Name the blood parasite species.
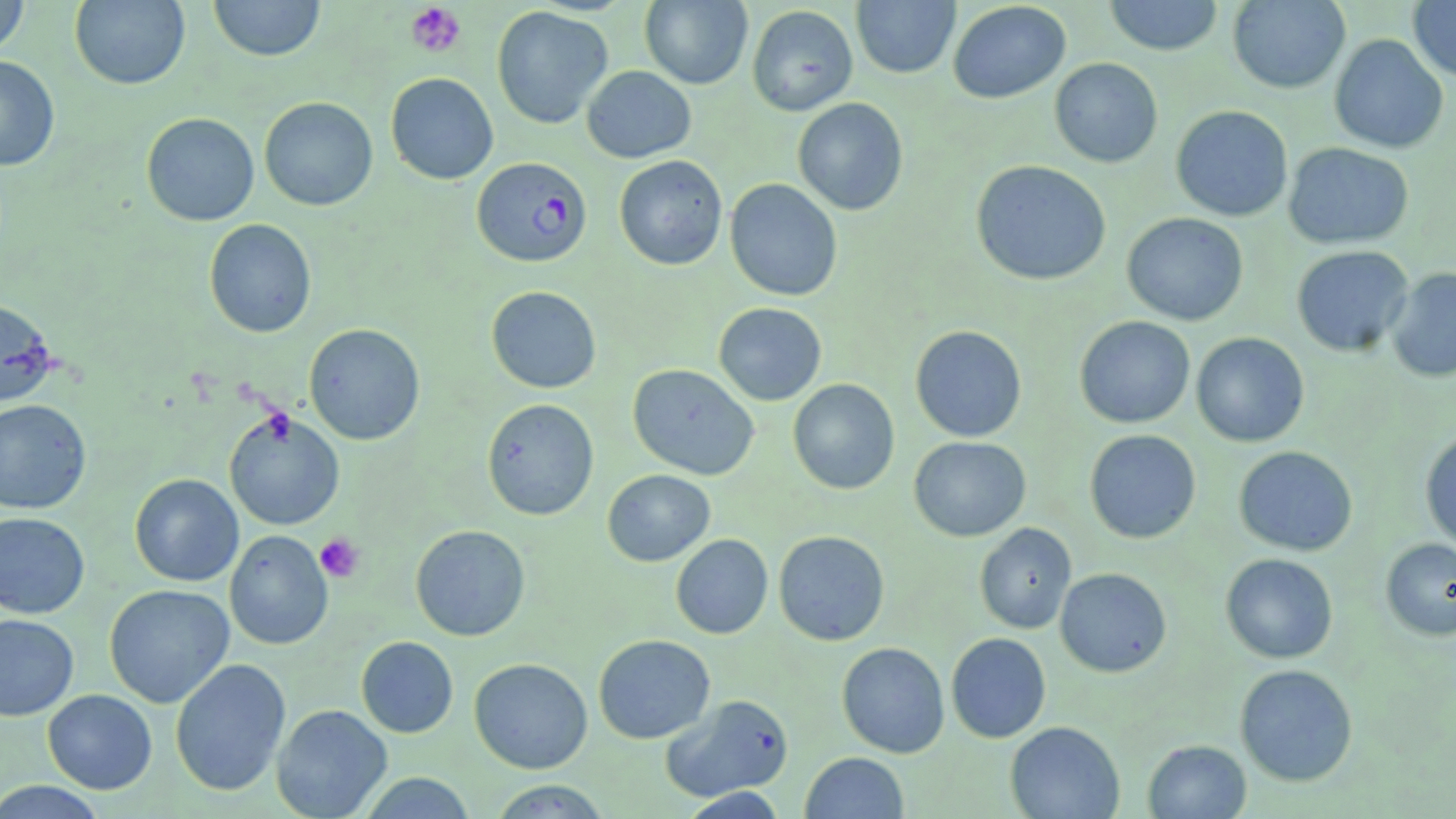
Plasmodium falciparum.

Summary:
  - Coordinate format: approximate bounding boxes as (x1, y1, x2, y2) in pixels
  - Plasmodium falciparum-infected red blood cell locations: (472, 158, 592, 268)
  - Uninfected red blood cell locations: (0, 0, 30, 58), (69, 0, 190, 90), (208, 0, 326, 62), (851, 0, 960, 79), (1104, 0, 1223, 56), (1227, 0, 1350, 94), (639, 1, 753, 89), (947, 1, 1071, 104), (1407, 1, 1456, 81), (491, 5, 612, 129), (747, 5, 858, 116), (1329, 33, 1449, 154), (0, 55, 60, 171), (1049, 57, 1163, 168), (581, 65, 696, 163), (385, 72, 498, 185), (258, 97, 378, 211), (792, 98, 908, 216), (1170, 105, 1293, 222), (141, 112, 260, 226), (1283, 142, 1414, 249), (614, 155, 728, 270), (970, 160, 1112, 286), (724, 178, 843, 301), (1121, 212, 1249, 326), (203, 218, 316, 338), (1290, 245, 1414, 357), (1387, 267, 1456, 383), (486, 285, 601, 393), (0, 297, 58, 407), (713, 302, 827, 406), (1074, 316, 1195, 428), (304, 323, 425, 445), (909, 325, 1027, 442), (1190, 332, 1309, 448), (628, 363, 759, 480), (787, 378, 900, 495), (482, 398, 599, 521), (0, 399, 92, 514), (224, 410, 345, 530), (1084, 429, 1201, 543), (1420, 429, 1456, 551), (908, 436, 1031, 541), (1233, 446, 1358, 556), (602, 469, 715, 567), (129, 474, 243, 586), (0, 511, 90, 618), (974, 522, 1077, 634), (410, 524, 530, 641), (224, 530, 333, 650), (773, 530, 890, 646), (671, 534, 773, 639), (1380, 537, 1456, 642), (1220, 553, 1338, 663), (1055, 568, 1172, 677), (104, 584, 234, 708), (0, 614, 79, 720), (946, 632, 1051, 743), (593, 634, 715, 744), (356, 636, 458, 738), (836, 642, 950, 758), (469, 657, 593, 774), (170, 658, 291, 797), (1234, 664, 1359, 787), (42, 689, 157, 794), (661, 694, 794, 802), (271, 704, 392, 818), (1005, 721, 1125, 819), (1142, 740, 1252, 819), (800, 752, 909, 818), (357, 772, 477, 818), (487, 780, 613, 818), (0, 781, 109, 818), (678, 787, 788, 818)
  - Platelet locations: (405, 2, 467, 58), (315, 533, 365, 583)
  - Stain: May-Grünwald-Giemsa
  - Magnification: 1000x
  - Image size: 1456×819 pixels
  - Modality: optical microscopy
  - Preparation: thin blood film
  - Field of view: single